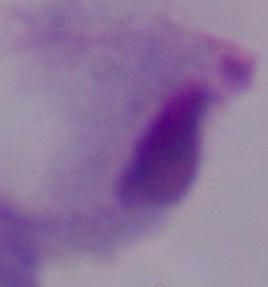
Photomicrograph. A trichomonad is shown. Captured at 1000x magnification.